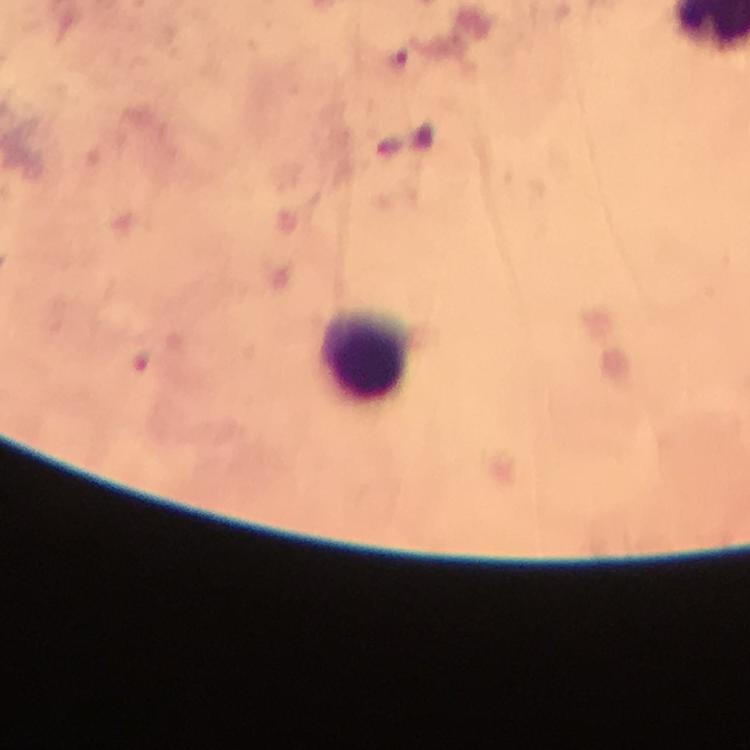

immersion oil = applied
preparation = thick blood film
cropped from = one field of view
context = from a diagnostic examination for malaria
leukocyte locations = approximate centers as (x, y) in pixels: (363, 351)
magnification = 100x
image size = 750×750 pixels
capture = smartphone photograph through a microscope
stain = Giemsa
malaria parasite locations = approximate centers as (x, y) in pixels: (400, 59)